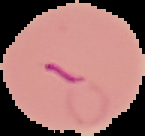
result = Plasmodium parasites identified
image type = segmented cell region on a black background
preparation = thin blood smear
image size = 145×136 pixels